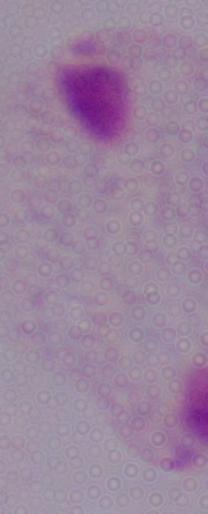
modality = micrograph
identification = trichomonad
magnification = 1000x